Give the position of every malaria parasite.
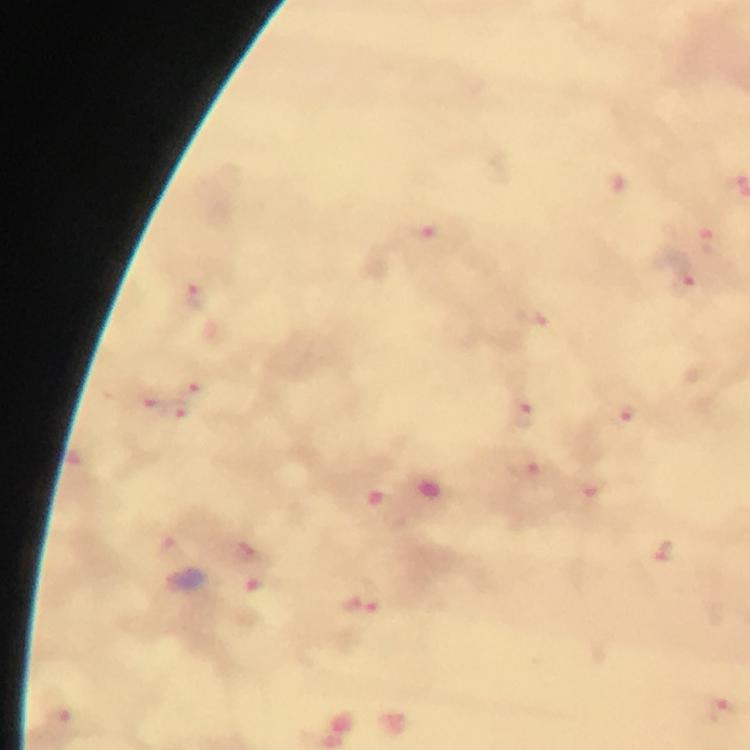

Approximate centers as (x, y) in pixels.
Malaria parasites: (424, 238), (706, 240), (683, 284), (196, 297), (196, 382), (145, 398), (179, 409), (625, 415), (525, 416), (528, 467), (248, 550), (665, 551), (363, 605), (724, 711).

Thick smear. 100x magnification. Giemsa stain. Image is 750×750 pixels. From a malaria diagnostic workup. A crop from one field of view. Immersion oil applied. Smartphone photograph taken through a microscope.